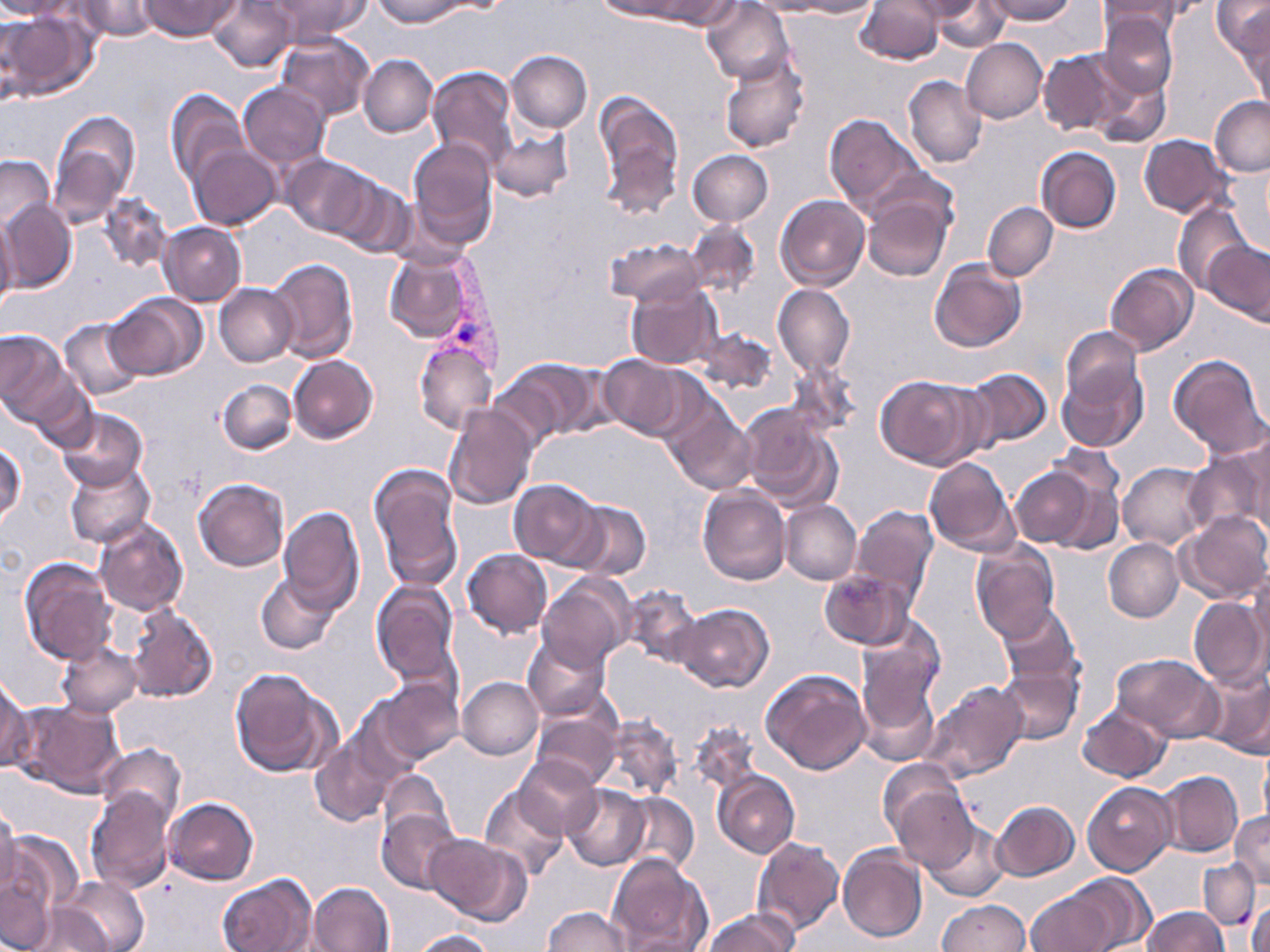
slide_level_diagnosis: Plasmodium vivax
image_size: 1270×952 pixels
uninfected_red_blood_cell_locations: 'approximate bounding boxes as (x1, y1, x2, y2) in pixels: (0, 0, 80, 19), (74, 0, 161, 40), (140, 0, 239, 40), (205, 0, 296, 71), (266, 0, 369, 43), (371, 0, 466, 27), (593, 0, 694, 22), (742, 0, 833, 16), (794, 0, 878, 18), (904, 0, 987, 20), (983, 0, 1075, 24), (641, 1, 743, 29), (702, 1, 795, 86), (856, 1, 944, 65), (933, 1, 1007, 51), (1098, 1, 1186, 37), (1212, 1, 1270, 56), (1232, 3, 1269, 100), (1, 8, 97, 102), (1097, 10, 1178, 97), (275, 31, 375, 121), (961, 38, 1047, 124), (1038, 49, 1131, 137), (505, 50, 592, 132), (719, 53, 811, 155), (358, 54, 437, 136), (425, 66, 518, 170), (1087, 70, 1171, 149), (903, 75, 987, 168), (238, 82, 330, 170), (165, 88, 248, 186), (592, 90, 685, 217), (1209, 95, 1270, 177), (48, 110, 140, 225), (825, 113, 923, 215), (487, 127, 574, 201), (1140, 135, 1234, 219), (407, 139, 497, 244), (189, 144, 281, 231), (1035, 146, 1120, 233), (688, 150, 773, 226), (0, 154, 55, 236), (282, 154, 378, 238), (334, 175, 415, 257), (860, 188, 954, 281), (100, 195, 172, 272), (776, 195, 870, 291), (1, 199, 77, 292), (983, 202, 1058, 281), (1173, 202, 1254, 295), (0, 216, 18, 315), (684, 221, 760, 296), (157, 222, 247, 306), (604, 238, 705, 306), (1204, 239, 1270, 326), (382, 251, 481, 344), (266, 258, 359, 363), (930, 260, 1027, 354), (1105, 263, 1198, 356), (627, 282, 722, 370), (214, 283, 297, 367), (772, 284, 855, 377), (105, 293, 208, 382), (58, 317, 145, 403), (693, 327, 776, 395), (0, 329, 71, 423), (1061, 329, 1143, 416), (414, 339, 497, 435), (1166, 353, 1268, 460), (289, 354, 378, 444), (597, 354, 688, 438), (496, 357, 604, 444), (1056, 361, 1148, 455), (961, 367, 1053, 450), (875, 375, 982, 469), (218, 379, 297, 454), (442, 403, 538, 508), (665, 406, 756, 494), (740, 406, 843, 512), (55, 408, 148, 492), (1240, 432, 1270, 534), (1, 441, 26, 528), (1185, 445, 1268, 537), (923, 456, 1019, 557), (369, 461, 464, 592), (1117, 461, 1210, 548), (65, 462, 156, 549), (1009, 465, 1100, 550), (193, 477, 289, 572), (509, 479, 602, 567), (697, 487, 791, 585), (564, 500, 651, 581), (779, 500, 861, 585), (278, 506, 365, 613), (850, 506, 939, 605), (1178, 511, 1270, 603), (95, 520, 188, 615), (1103, 538, 1184, 622), (970, 542, 1059, 643), (461, 549, 552, 638), (19, 556, 117, 665), (820, 568, 915, 649), (256, 571, 341, 655), (539, 575, 633, 668), (1249, 575, 1270, 668), (371, 581, 459, 686), (621, 584, 703, 667), (1188, 596, 1268, 688), (997, 602, 1081, 685), (674, 603, 774, 693), (123, 604, 218, 703), (856, 628, 943, 752), (523, 633, 611, 723), (56, 640, 142, 718), (1111, 653, 1222, 740), (997, 662, 1082, 744), (1198, 664, 1270, 759), (230, 668, 339, 779), (761, 668, 872, 775), (0, 674, 31, 772), (458, 676, 543, 760), (374, 679, 464, 764), (922, 680, 1029, 784), (349, 697, 428, 785), (11, 699, 126, 797), (1078, 702, 1170, 783), (531, 707, 621, 787), (599, 717, 682, 799), (688, 720, 762, 797), (310, 735, 396, 826), (97, 742, 186, 828), (514, 756, 604, 839), (378, 770, 455, 846), (1158, 770, 1243, 858), (712, 771, 800, 858), (883, 771, 977, 872), (1082, 782, 1176, 875), (478, 784, 568, 881), (562, 785, 651, 871), (86, 787, 176, 894), (619, 793, 700, 875), (164, 797, 257, 886), (991, 800, 1079, 881), (0, 805, 22, 898), (376, 808, 462, 894), (1229, 811, 1270, 888), (923, 819, 1008, 902), (3, 828, 81, 933), (934, 830, 1019, 950), (426, 835, 532, 927), (752, 837, 844, 937), (836, 844, 928, 943), (606, 852, 714, 952), (1199, 858, 1262, 929), (0, 867, 57, 952), (56, 874, 148, 952), (217, 874, 313, 952), (309, 883, 394, 952), (1025, 886, 1122, 952), (1248, 893, 1269, 952), (938, 899, 1030, 951), (26, 902, 110, 951), (544, 906, 631, 952), (1141, 907, 1229, 952), (702, 909, 797, 952), (410, 929, 495, 952)'
field_of_view: single
plasmodium_vivax_infected_red_blood_cell_locations: 'approximate bounding boxes as (x1, y1, x2, y2) in pixels: (429, 249, 510, 378)'
preparation: thin blood film
modality: light microscopy
stain: May-Grünwald-Giemsa
magnification: 1000x